Assess this cell for malaria.
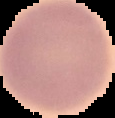

Uninfected.

preparation = thin blood film
image size = 115×118 pixels
image type = segmented cell region on a black background